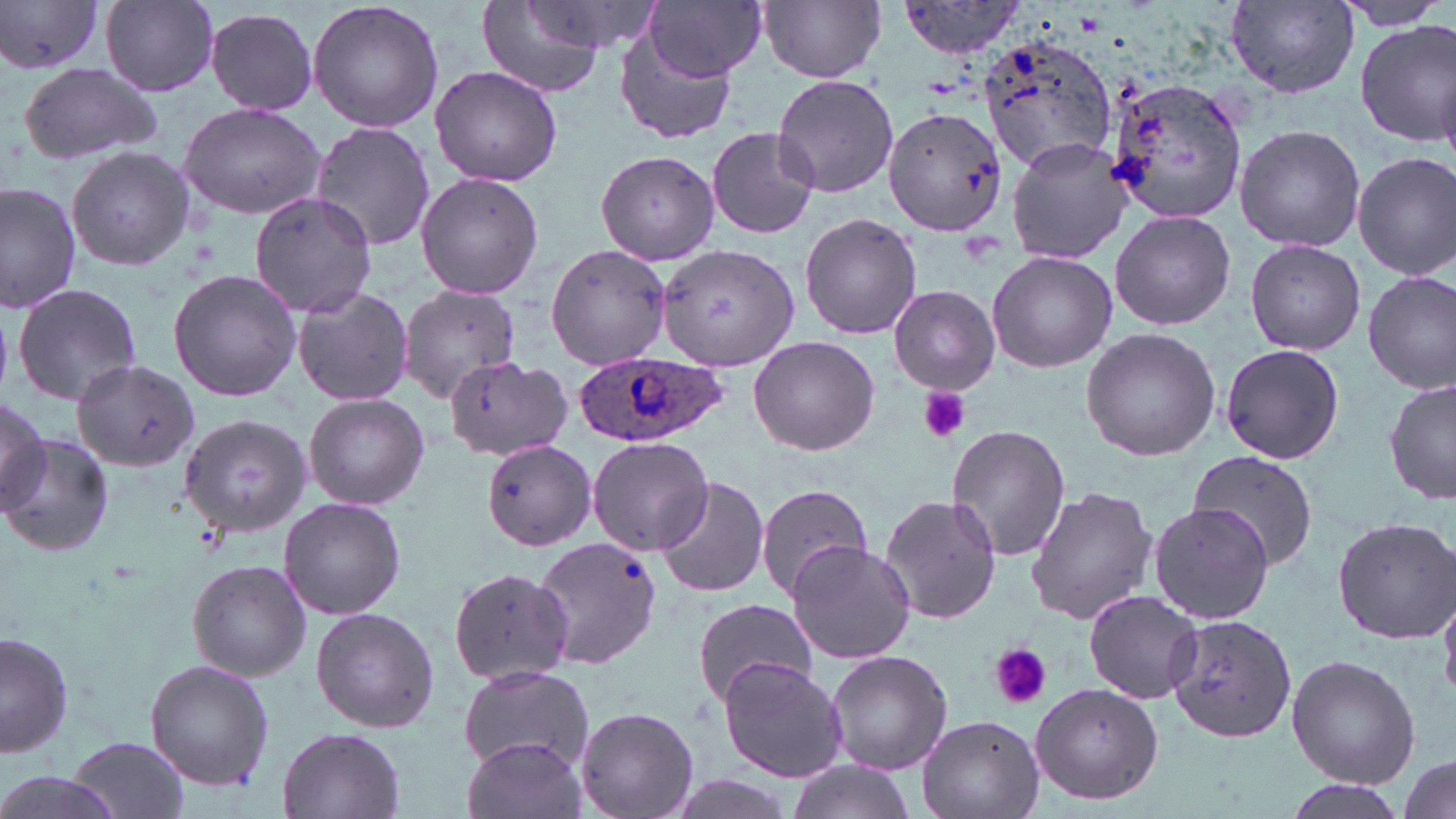
Summary:
  - Coordinate format: approximate bounding boxes as (x1,y1)-(x2,y2) corner pairs in pixels
  - Uninfected red blood cell locations: (1,0)-(102,76), (307,0)-(444,134), (646,0)-(768,81), (760,0)-(886,83), (1330,0)-(1454,31), (898,1)-(1029,58), (1226,1)-(1360,97), (101,2)-(219,96), (477,2)-(607,97), (204,6)-(321,116), (1356,21)-(1456,146), (614,27)-(738,148), (985,34)-(1118,223), (19,62)-(161,165), (430,65)-(563,186), (773,73)-(900,199), (1101,76)-(1248,222), (176,100)-(327,220), (882,105)-(1005,236), (309,121)-(437,251), (1234,125)-(1365,252), (706,126)-(819,239), (1005,138)-(1132,264), (66,146)-(194,273), (595,149)-(721,266), (1352,150)-(1456,280), (416,173)-(544,298), (1,181)-(82,314), (249,191)-(378,317), (1109,210)-(1236,330), (799,213)-(923,339), (1244,240)-(1365,354), (548,243)-(669,368), (656,243)-(799,370), (986,250)-(1116,373), (169,270)-(302,401), (1363,270)-(1456,392), (888,284)-(1001,394), (13,285)-(144,407), (291,286)-(414,407), (396,286)-(523,403), (1081,326)-(1220,462), (748,335)-(880,457), (1219,342)-(1345,464), (438,357)-(564,463), (71,359)-(201,472), (1384,378)-(1455,505), (0,393)-(50,514), (304,393)-(431,510), (179,413)-(311,535), (948,425)-(1071,561), (2,433)-(114,558), (586,434)-(714,556), (480,440)-(595,550), (1189,453)-(1319,571), (654,473)-(770,600), (752,483)-(875,604), (1026,485)-(1161,624), (879,492)-(1002,626), (280,498)-(405,619), (1147,501)-(1277,626), (1331,517)-(1455,642), (532,535)-(663,672), (785,540)-(916,664), (186,559)-(312,683), (450,568)-(575,683), (1083,589)-(1203,705), (692,597)-(817,706), (308,607)-(439,732), (1166,613)-(1298,742), (1,629)-(75,759), (825,649)-(953,776), (1285,655)-(1421,790), (717,657)-(848,784), (145,660)-(274,791), (458,664)-(593,772), (1028,683)-(1165,807), (575,705)-(699,819), (916,713)-(1043,819), (277,727)-(405,819), (461,734)-(587,819), (69,735)-(190,817), (1396,755)-(1453,816), (783,762)-(917,819), (0,770)-(124,819)
  - Platelet locations: (917,387)-(970,443), (989,645)-(1050,709)
  - Plasmodium ovale-infected red blood cell locations: (573,348)-(727,448)
  - Slide-level diagnosis: Plasmodium ovale
  - Field of view: single
  - Magnification: 1000x
  - Stain: May-Grünwald-Giemsa
  - Image size: 1456×819 pixels
  - Modality: optical microscopy
  - Preparation: thin blood film